Report the malaria status of this cell.
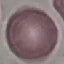
It is uninfected.

Summary:
  - Preparation: thin blood smear
  - Image type: cell patch, automatically extracted from a larger field of view and resized to 64 × 64 pixels
  - Capture: smartphone camera at the microscope eyepiece
  - Stain: Giemsa